Give the extent of all Plasmodium falciparum-infected red blood cells.
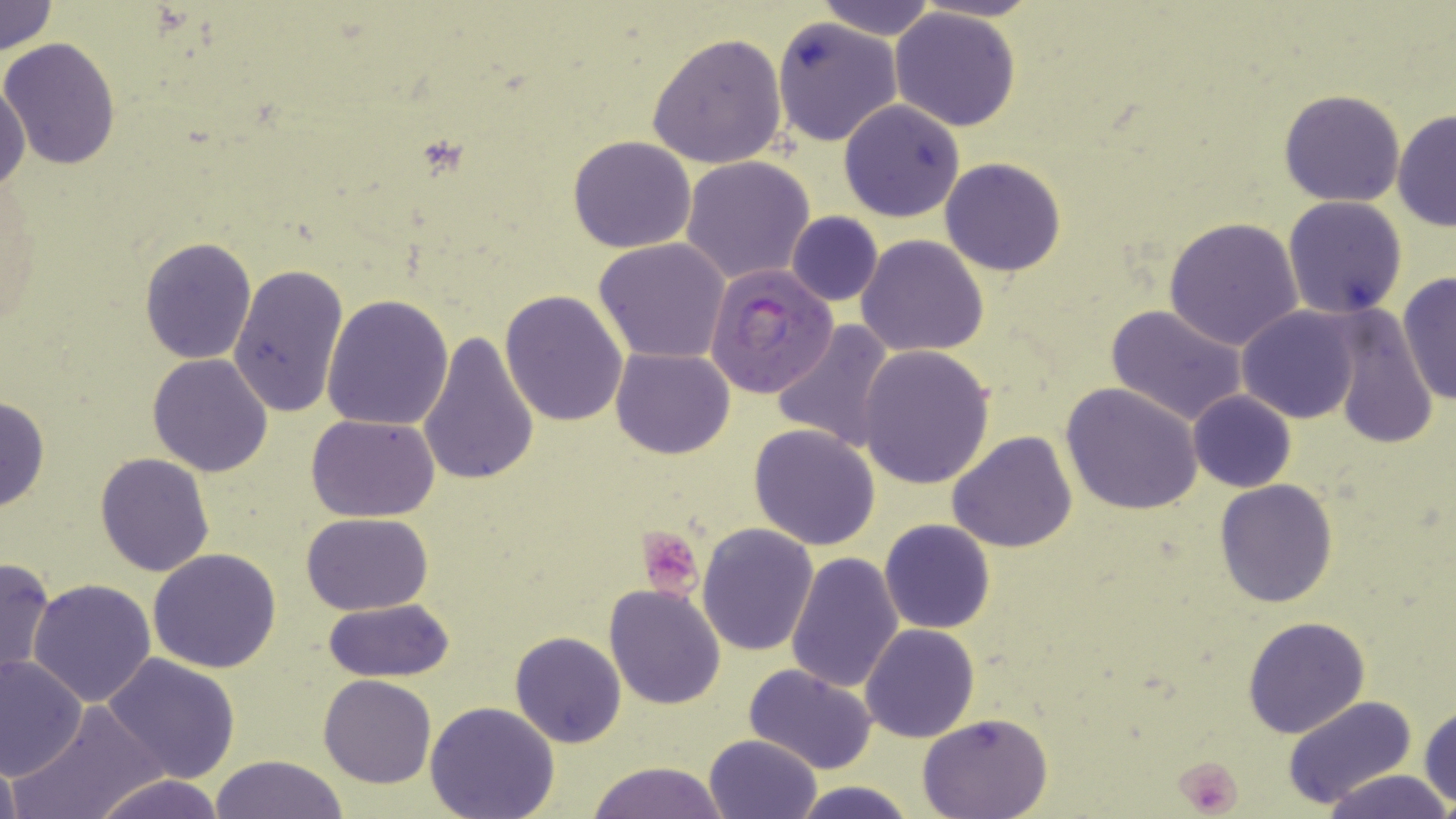
Approximate bounding boxes as (x1,y1)-(x2,y2) corner pairs in pixels.
Plasmodium falciparum-infected red blood cells: (705,262)-(837,395).

Platelet locations: (634,527)-(707,598), (1174,757)-(1244,816). Uninfected red blood cell locations: (0,0)-(58,57), (815,0)-(939,39), (889,8)-(1023,131), (773,18)-(900,147), (646,33)-(789,170), (0,38)-(121,170), (0,77)-(29,193), (1278,89)-(1406,207), (839,101)-(965,222), (1391,109)-(1455,232), (568,135)-(697,254), (680,156)-(818,286), (941,157)-(1067,276), (1282,195)-(1408,319), (786,212)-(883,307), (1163,217)-(1305,352), (857,235)-(988,356), (140,237)-(256,363), (594,237)-(733,363), (227,264)-(349,419), (1397,271)-(1456,407), (501,290)-(629,428), (323,294)-(453,431), (1105,305)-(1249,427), (1237,307)-(1364,423), (1326,310)-(1440,450), (771,320)-(897,453), (420,331)-(540,487), (856,345)-(995,488), (612,347)-(733,460), (148,354)-(274,477), (1060,381)-(1205,517), (1188,390)-(1296,493), (1,395)-(49,514), (306,414)-(442,523), (748,425)-(880,550), (947,432)-(1078,553), (95,452)-(215,576), (1215,479)-(1339,608), (301,512)-(436,615), (880,519)-(996,635), (697,522)-(818,656), (148,548)-(281,673), (785,551)-(904,693), (0,556)-(55,682), (28,577)-(159,707), (604,585)-(725,710), (322,596)-(453,683), (1242,616)-(1370,739), (860,624)-(979,743), (510,631)-(627,747), (0,652)-(88,779), (101,653)-(239,783), (744,665)-(878,777), (319,675)-(436,788), (1280,695)-(1416,811), (11,701)-(168,819), (425,701)-(560,819), (1419,703)-(1456,810), (919,714)-(1053,819), (703,734)-(821,819), (0,753)-(25,817), (210,755)-(351,818), (585,760)-(731,818), (1324,769)-(1451,819), (91,772)-(226,819), (789,779)-(917,819). Slide-level diagnosis: Plasmodium falciparum. May-Grünwald-Giemsa stain. Image is 1456×819 pixels. Single field of view. Thin blood film. Light microscopy. Captured at 1000x magnification.